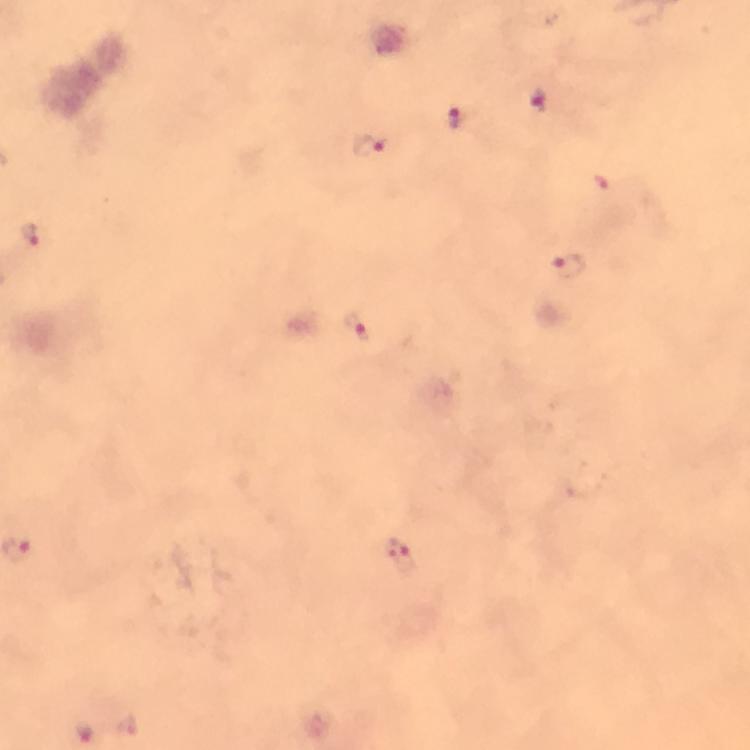
stain = Giemsa
context = from a diagnostic examination for malaria
magnification = 100x
cropped from = one field of view
preparation = thick blood smear
immersion oil = used
Plasmodium parasite locations = approximate centers as [x, y] in pixels: [538, 102], [455, 119], [369, 146], [32, 234], [566, 266], [357, 329], [398, 554], [126, 727], [84, 730]
capture = smartphone mounted on the microscope
image size = 750×750 pixels